Point out each Plasmodium parasite.
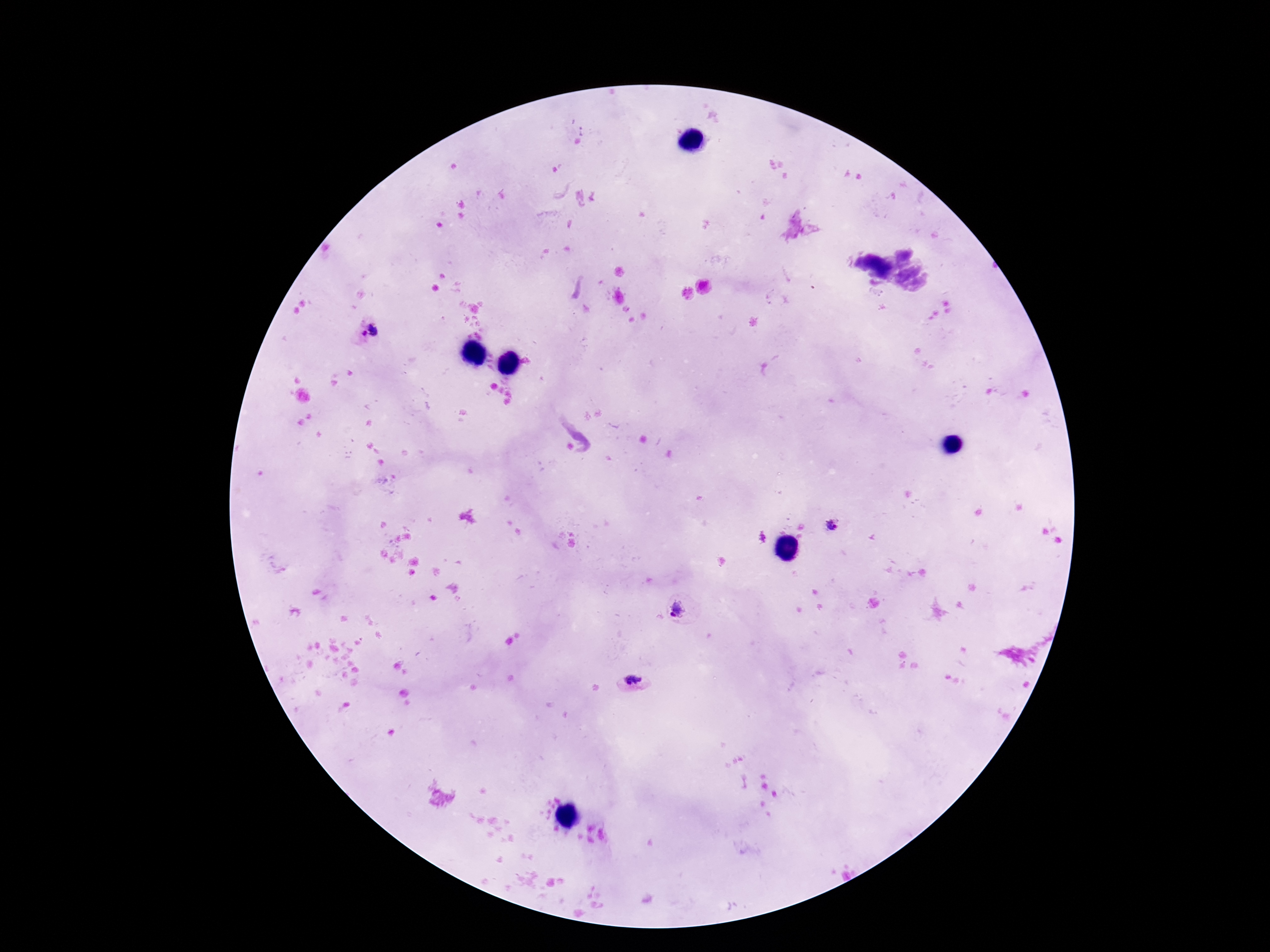
Approximate object centers, in pixels from the top-left corner.
Plasmodium parasites: (x=369, y=332), (x=835, y=524), (x=679, y=610), (x=632, y=683).

Summary:
  - Preparation: thick peripheral-blood smear
  - Capture: smartphone camera through the microscope eyepiece
  - Stain: Giemsa
  - Field of view: one from this slide
  - Image size: 1270×952 pixels
  - Magnification: 100x
  - Patient malaria status: positive